Name the parasite shown.
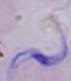

This is a trypanosome.

Photomicrograph. 1000x magnification.